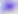

Captured at 400x magnification. Toxoplasma gondii is shown. Micrograph.